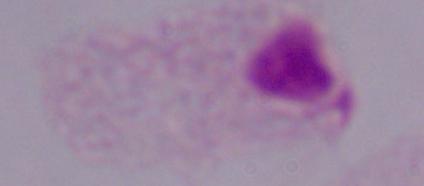
A trichomonad is seen. Photomicrograph. 1000x magnification.